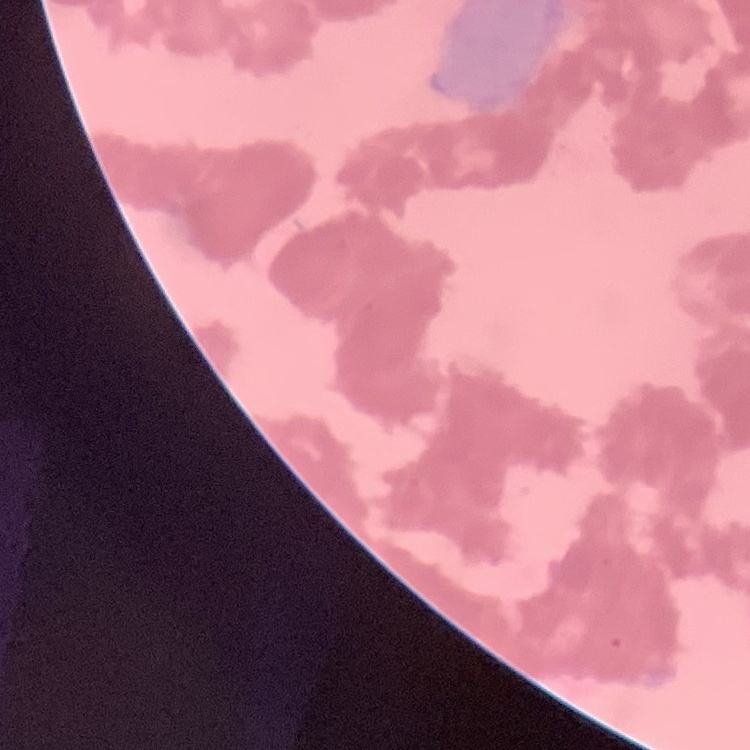 The erythrocytes exhibit rouleaux formation. One tile cut from a larger photomicrograph. Thin blood smear. Stained with either Field's or Giemsa.